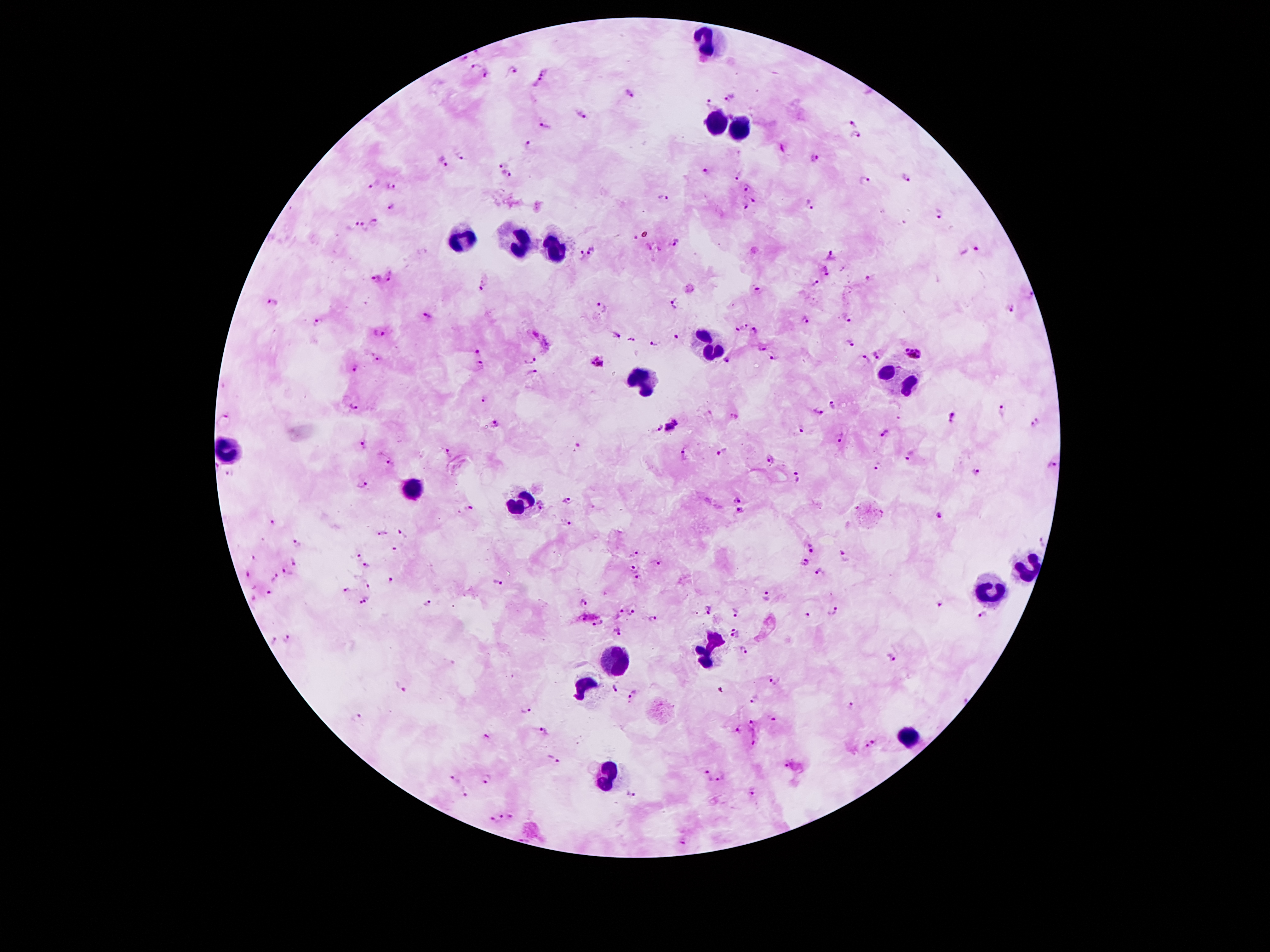 Approximate centers as [x, y] in pixels. Malaria parasite locations: [464, 57], [474, 65], [513, 70], [544, 71], [485, 73], [539, 81], [630, 92], [728, 96], [710, 105], [582, 116], [851, 122], [543, 126], [855, 137], [530, 143], [460, 155], [814, 156], [443, 162], [503, 163], [704, 169], [739, 172], [508, 175], [905, 178], [866, 180], [375, 183], [393, 186], [744, 186], [664, 197], [751, 197], [392, 206], [812, 206], [744, 207], [937, 214], [376, 221], [353, 224], [364, 228], [676, 242], [977, 249], [593, 251], [832, 256], [582, 257], [826, 271], [392, 277], [378, 279], [485, 283], [816, 284], [759, 289], [1031, 295], [273, 302], [674, 304], [603, 306], [1011, 308], [428, 316], [806, 321], [849, 321], [316, 324], [742, 328], [756, 329], [379, 334], [618, 335], [675, 335], [632, 340], [654, 344], [849, 344], [763, 349], [478, 351], [913, 352], [877, 354], [774, 356], [376, 359], [527, 359], [867, 360], [597, 361], [727, 361], [480, 365], [355, 369], [533, 372], [484, 398], [353, 404], [836, 405], [1001, 410], [819, 412], [733, 415], [898, 418], [953, 418], [1036, 422], [496, 424], [671, 427], [658, 428], [802, 430], [884, 434], [842, 437], [363, 444], [577, 447], [684, 452], [719, 452], [911, 453], [449, 454], [769, 458], [1053, 464], [389, 465], [877, 465], [976, 472], [229, 473], [797, 478], [360, 483], [737, 499], [568, 500], [469, 509], [742, 510], [942, 516], [273, 522], [566, 523], [383, 534], [404, 534], [1042, 540], [298, 543], [811, 549], [396, 550], [634, 554], [844, 555], [355, 556], [255, 559], [295, 561], [806, 562], [657, 563], [368, 564], [632, 568], [819, 571], [289, 572], [249, 575], [640, 577], [274, 579], [392, 581], [496, 581], [368, 584], [255, 585], [346, 590], [269, 592], [766, 594], [253, 599], [368, 600], [358, 602], [583, 602], [427, 603], [940, 607], [834, 608], [707, 609], [630, 611], [617, 612], [733, 612], [807, 614], [983, 614], [584, 618], [650, 618], [597, 622], [730, 627], [617, 631], [736, 637], [274, 639], [289, 639], [744, 650], [890, 657], [776, 680], [401, 686], [617, 686], [632, 695], [754, 699], [851, 705], [525, 709], [357, 718], [775, 719], [750, 724], [736, 729], [546, 731], [488, 735], [755, 737], [873, 742], [863, 746], [553, 760], [785, 766], [707, 776], [723, 777], [488, 779], [455, 780], [464, 792], [754, 792], [630, 794], [501, 815], [512, 816], [494, 820], [683, 842]. Leukocyte locations: [710, 44], [715, 124], [739, 128], [460, 242], [512, 246], [556, 251], [707, 348], [898, 383], [644, 387], [228, 448], [413, 487], [521, 507], [1023, 569], [987, 589], [705, 651], [617, 658], [587, 687], [908, 737], [605, 778]. Smartphone photograph taken through the microscope eyepiece. Image is 1270×952 pixels. Thick blood film. Giemsa stain. Single field of view. Patient malaria status: infected with Plasmodium falciparum. 100x magnification.